Identify the blood parasite species.
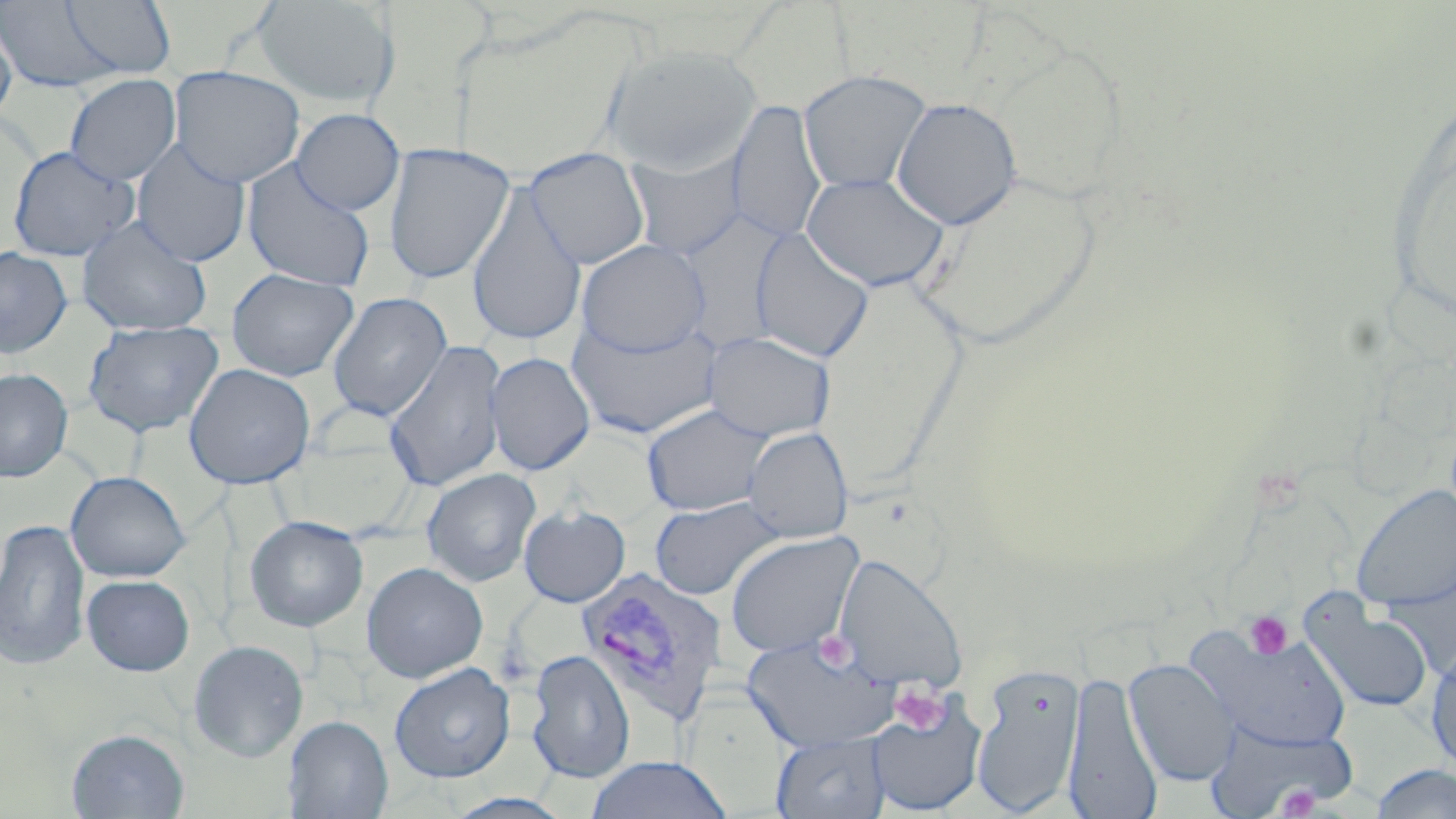
Plasmodium vivax.

Approximate bounding boxes as (x1, y1, x2, y2) in pixels. Uninfected red blood cell locations: (249, 0, 401, 108), (0, 1, 135, 94), (57, 1, 177, 80), (0, 15, 17, 128), (981, 31, 1134, 211), (602, 44, 762, 175), (168, 65, 305, 188), (798, 69, 932, 194), (64, 74, 181, 186), (891, 97, 1023, 230), (726, 100, 826, 244), (291, 109, 405, 215), (131, 139, 251, 267), (383, 143, 515, 285), (7, 146, 140, 262), (525, 148, 650, 270), (626, 149, 747, 260), (241, 159, 376, 291), (913, 170, 1106, 349), (800, 172, 951, 292), (466, 182, 587, 347), (77, 216, 212, 336), (749, 226, 875, 363), (576, 239, 711, 356), (0, 246, 73, 357), (226, 268, 359, 381), (327, 292, 452, 421), (567, 316, 720, 439), (82, 320, 224, 438), (703, 330, 836, 443), (383, 340, 507, 493), (486, 351, 595, 476), (184, 363, 315, 489), (0, 368, 73, 482), (641, 403, 772, 516), (744, 426, 853, 543), (422, 469, 541, 587), (65, 471, 190, 582), (1352, 483, 1456, 611), (650, 497, 783, 601), (519, 506, 631, 607), (244, 515, 369, 632), (0, 518, 90, 670), (725, 531, 863, 659), (834, 553, 966, 692), (361, 561, 488, 683), (82, 575, 195, 676), (1300, 596, 1433, 714), (1187, 624, 1351, 751), (743, 633, 896, 751), (188, 640, 309, 762), (1426, 644, 1456, 775), (525, 649, 636, 782), (1123, 657, 1240, 786), (389, 662, 515, 782), (971, 663, 1085, 815), (1063, 670, 1163, 817), (867, 694, 988, 816), (284, 715, 393, 818), (1203, 716, 1358, 817), (66, 728, 190, 818), (771, 731, 891, 818), (587, 755, 732, 818), (1368, 763, 1456, 819). Platelet locations: (1243, 610, 1293, 659), (890, 682, 949, 736), (1275, 785, 1325, 817). Plasmodium vivax-infected red blood cell locations: (575, 566, 727, 726). 1000x magnification. Image is 1456×819 pixels. May-Grünwald-Giemsa-stained preparation. Optical microscopy. One field of a larger specimen. Thin blood film.